Locate every malaria parasite.
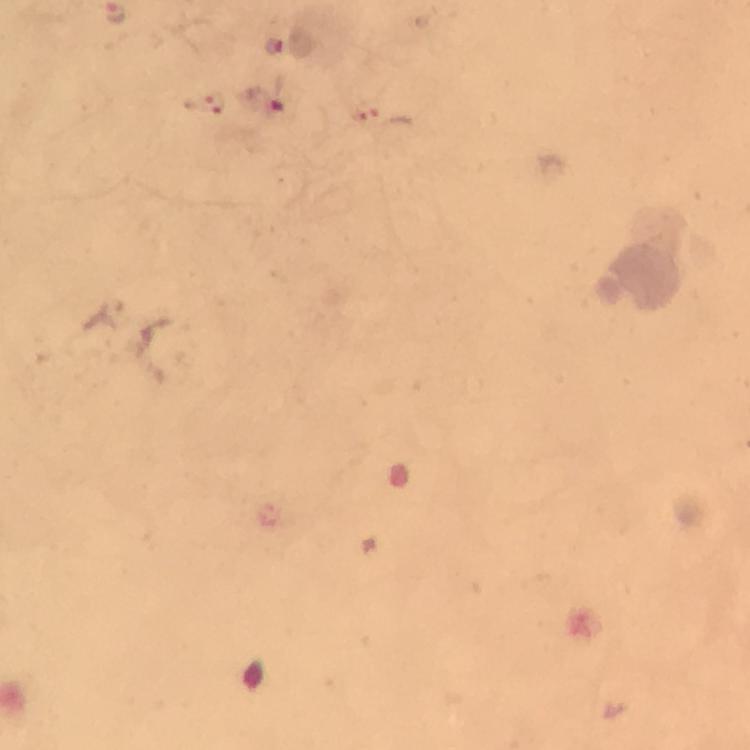

Approximate centers as (x, y) in pixels.
Malaria parasites: (273, 46), (215, 102), (264, 102).

{
  "stain": "Giemsa",
  "context": "from a malaria diagnostic workup",
  "immersion_oil": "used",
  "preparation": "thick blood smear",
  "image_size": "750×750 pixels",
  "cropped_from": "one field of view",
  "capture": "smartphone photograph through a microscope",
  "magnification": "100x"
}